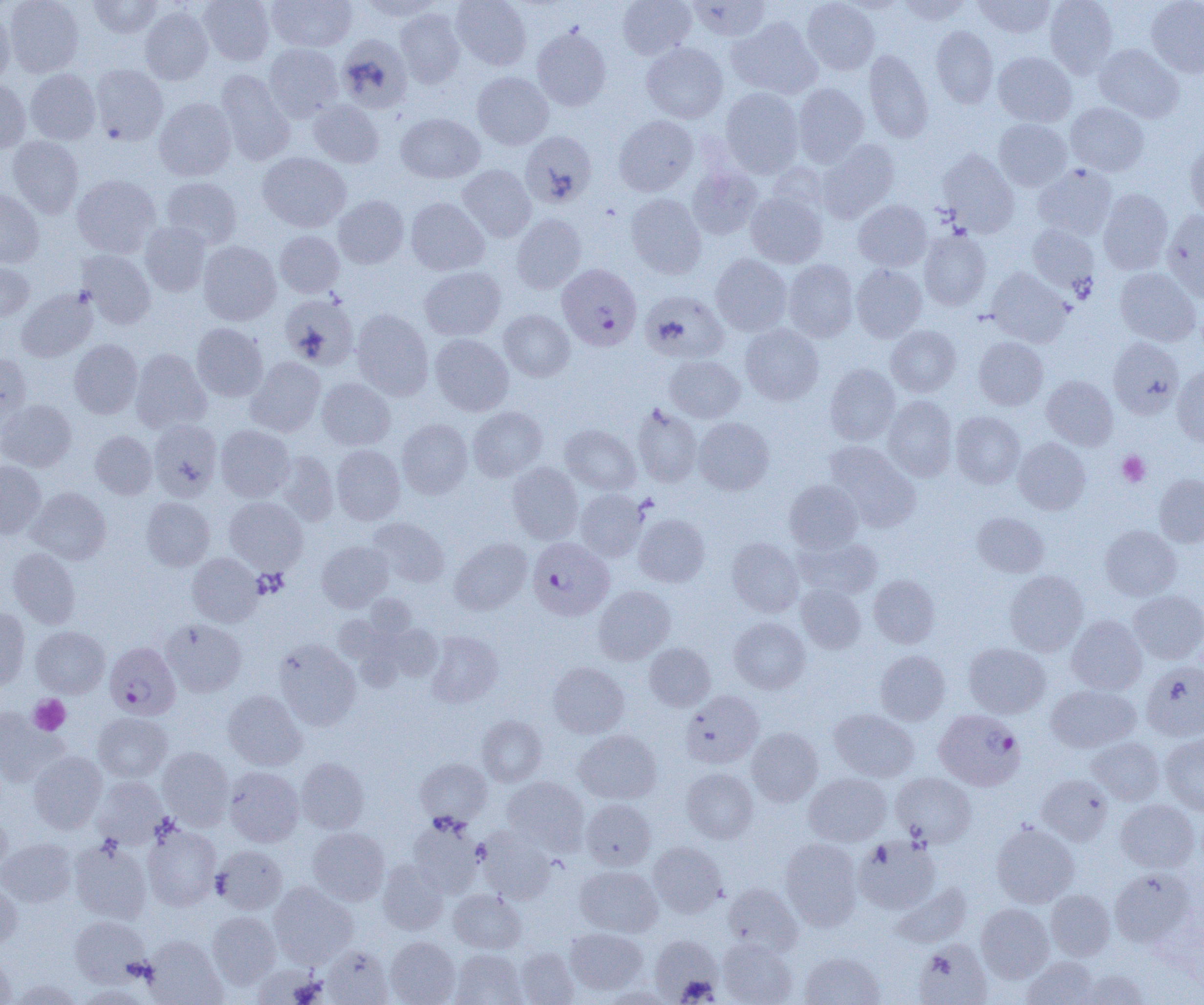 Approximate bounding boxes as (x1, y1, x2, y2) in pixels. Platelet locations: (1117, 451, 1150, 486), (252, 568, 288, 599), (29, 695, 70, 735). Plasmodium falciparum-infected red blood cell locations: (560, 262, 647, 353), (527, 536, 620, 618), (105, 641, 180, 720), (934, 709, 1025, 791). Uninfected red blood cell locations: (4, 0, 84, 77), (88, 0, 162, 38), (197, 0, 275, 66), (267, 0, 357, 52), (357, 0, 441, 21), (451, 0, 531, 70), (618, 0, 696, 60), (687, 0, 770, 41), (802, 0, 879, 75), (897, 0, 972, 25), (973, 0, 1056, 38), (1044, 0, 1118, 77), (1146, 0, 1204, 78), (139, 5, 213, 85), (0, 8, 15, 85), (395, 8, 465, 88), (727, 17, 822, 99), (930, 25, 999, 108), (532, 26, 612, 111), (336, 35, 412, 113), (263, 43, 343, 121), (641, 43, 728, 123), (1094, 44, 1184, 122), (864, 49, 933, 143), (993, 51, 1076, 126), (90, 64, 168, 145), (25, 69, 101, 144), (215, 69, 296, 166), (471, 72, 553, 149), (0, 79, 31, 152), (792, 83, 869, 166), (720, 88, 804, 177), (154, 97, 236, 181), (308, 99, 384, 168), (1066, 102, 1149, 175), (396, 113, 485, 183), (614, 115, 698, 196), (993, 119, 1072, 190), (520, 131, 596, 208), (7, 136, 84, 218), (816, 139, 900, 223), (1184, 143, 1204, 221), (937, 150, 1019, 237), (257, 152, 351, 232), (1033, 164, 1117, 240), (457, 165, 536, 242), (687, 165, 763, 239), (72, 174, 160, 258), (162, 177, 242, 248), (1098, 188, 1173, 274), (0, 190, 44, 268), (746, 191, 828, 268), (626, 193, 706, 279), (333, 195, 409, 268), (406, 197, 489, 275), (854, 200, 932, 272), (1162, 210, 1204, 300), (512, 213, 586, 293), (140, 221, 211, 296), (1027, 224, 1099, 296), (275, 230, 344, 297), (919, 230, 991, 311), (198, 240, 281, 325), (78, 250, 156, 329), (711, 254, 792, 336), (783, 259, 858, 342), (0, 262, 34, 321), (851, 265, 927, 342), (420, 266, 506, 340), (986, 268, 1070, 347), (1115, 268, 1201, 346), (17, 287, 97, 362), (640, 291, 728, 363), (280, 294, 359, 370), (351, 309, 433, 400), (499, 309, 574, 381), (192, 323, 268, 401), (740, 324, 823, 405), (886, 325, 961, 397), (430, 334, 513, 416), (1107, 336, 1184, 418), (973, 337, 1048, 410), (69, 339, 142, 418), (130, 349, 211, 433), (0, 354, 32, 426), (664, 355, 744, 423), (246, 357, 326, 437), (825, 364, 900, 445), (1172, 366, 1204, 446), (1042, 376, 1117, 450), (317, 377, 395, 450), (882, 396, 957, 482), (0, 399, 77, 472), (632, 404, 702, 487), (468, 406, 547, 481), (950, 411, 1025, 489), (397, 415, 546, 489), (693, 417, 774, 495), (148, 419, 222, 500), (397, 419, 472, 498), (561, 424, 641, 494), (216, 425, 293, 502), (90, 431, 157, 499), (1013, 438, 1090, 514), (825, 441, 920, 531), (331, 445, 405, 524), (276, 450, 338, 525), (0, 461, 45, 538), (507, 462, 583, 544), (1154, 474, 1204, 547), (784, 480, 863, 553), (27, 487, 110, 564), (575, 488, 648, 561), (141, 497, 214, 570), (225, 497, 307, 573), (972, 511, 1048, 577), (634, 513, 710, 587), (368, 517, 449, 587), (1100, 525, 1181, 600), (796, 536, 883, 599), (727, 537, 803, 617), (450, 538, 532, 614), (317, 541, 393, 611), (8, 547, 80, 628), (187, 553, 263, 627), (1004, 570, 1088, 656), (868, 575, 940, 648), (797, 584, 866, 653), (593, 586, 675, 664), (1129, 590, 1204, 664), (362, 594, 416, 644), (0, 607, 30, 689), (1067, 615, 1147, 695), (729, 617, 810, 694), (161, 619, 246, 696), (386, 624, 442, 680), (31, 626, 109, 697), (426, 630, 503, 708), (274, 639, 360, 730), (964, 642, 1050, 718), (645, 643, 715, 711), (875, 650, 950, 725), (1141, 661, 1204, 741), (548, 662, 629, 738), (1046, 684, 1140, 752), (223, 690, 306, 770), (681, 690, 763, 767), (0, 709, 67, 787), (829, 709, 919, 782), (93, 712, 172, 782), (477, 715, 547, 786), (747, 728, 823, 806), (574, 729, 661, 804), (1160, 734, 1204, 815), (1087, 737, 1164, 805), (157, 746, 233, 829), (28, 750, 107, 833), (296, 758, 368, 833), (415, 758, 491, 825), (224, 766, 303, 846), (682, 768, 757, 843), (891, 772, 977, 847), (803, 773, 892, 846), (1037, 774, 1113, 846), (93, 776, 166, 846), (502, 776, 589, 854), (581, 799, 656, 870), (1116, 799, 1199, 872), (0, 813, 12, 877), (408, 817, 485, 898), (991, 822, 1079, 908), (142, 824, 221, 910), (307, 827, 390, 905), (478, 829, 557, 904), (853, 836, 941, 914), (780, 837, 863, 930), (0, 839, 76, 906), (69, 839, 152, 924), (648, 842, 727, 918), (212, 845, 287, 914), (377, 859, 449, 935), (575, 866, 662, 937), (1109, 868, 1196, 947), (269, 882, 357, 968), (890, 882, 973, 948), (0, 883, 22, 950), (723, 883, 801, 955), (448, 889, 525, 953), (1046, 890, 1115, 960), (976, 903, 1054, 982), (207, 911, 281, 988), (70, 915, 151, 986), (565, 927, 648, 994), (649, 934, 723, 1003), (143, 936, 226, 1005), (385, 936, 460, 1005), (717, 937, 797, 1005), (913, 939, 992, 1005), (320, 944, 394, 1004), (515, 947, 579, 1004), (451, 949, 526, 1005), (799, 952, 885, 1005), (0, 953, 17, 1004), (1022, 956, 1100, 1004), (251, 964, 324, 1005), (1075, 970, 1150, 1004), (10, 978, 83, 1004), (77, 985, 151, 1005), (601, 985, 676, 1004). Slide-level diagnosis: Plasmodium falciparum. Captured at 1000x magnification. Single field of view. Image is 1204×1005 pixels. Thin blood film. Light microscopy.